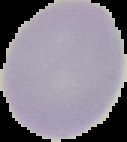
The area outside the segmented cell region is set to black. Malaria status: uninfected. Image is 127×142 pixels. From a thin blood smear.